State which cell type is depicted.
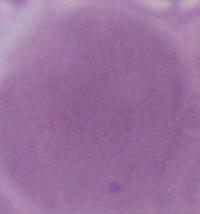
An erythrocyte.

modality = micrograph
magnification = 1000x